Classify this cell by malaria status.
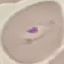

It is parasitized.

preparation = thin blood smear
image type = automatically extracted cell patch, resized to 64 × 64 pixels
capture = smartphone camera at the microscope eyepiece
stain = Giemsa